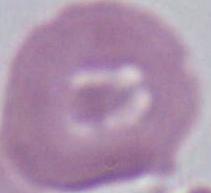 1000x magnification. An erythrocyte is shown. Photomicrograph.